Identify the cell.
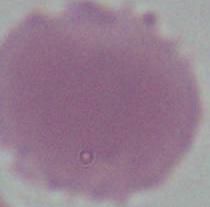
This is an erythrocyte.

Micrograph. Captured at 1000x magnification.